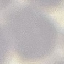

Malaria status: uninfected. Giemsa stain. Acquired by smartphone through the microscope eyepiece. Automatically extracted cell patch, resized to 64 × 64 pixels. Thin blood smear.